Identify the parasite.
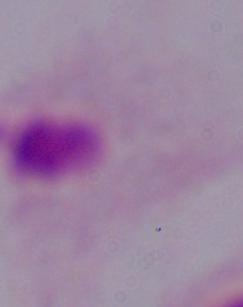
A trichomonad.

Photomicrograph. 1000x magnification.